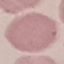
malaria status = uninfected
preparation = thin blood smear
image type = cell patch, automatically extracted from a larger field of view and resized to 64 × 64 pixels
capture = smartphone through the microscope eyepiece
stain = Giemsa